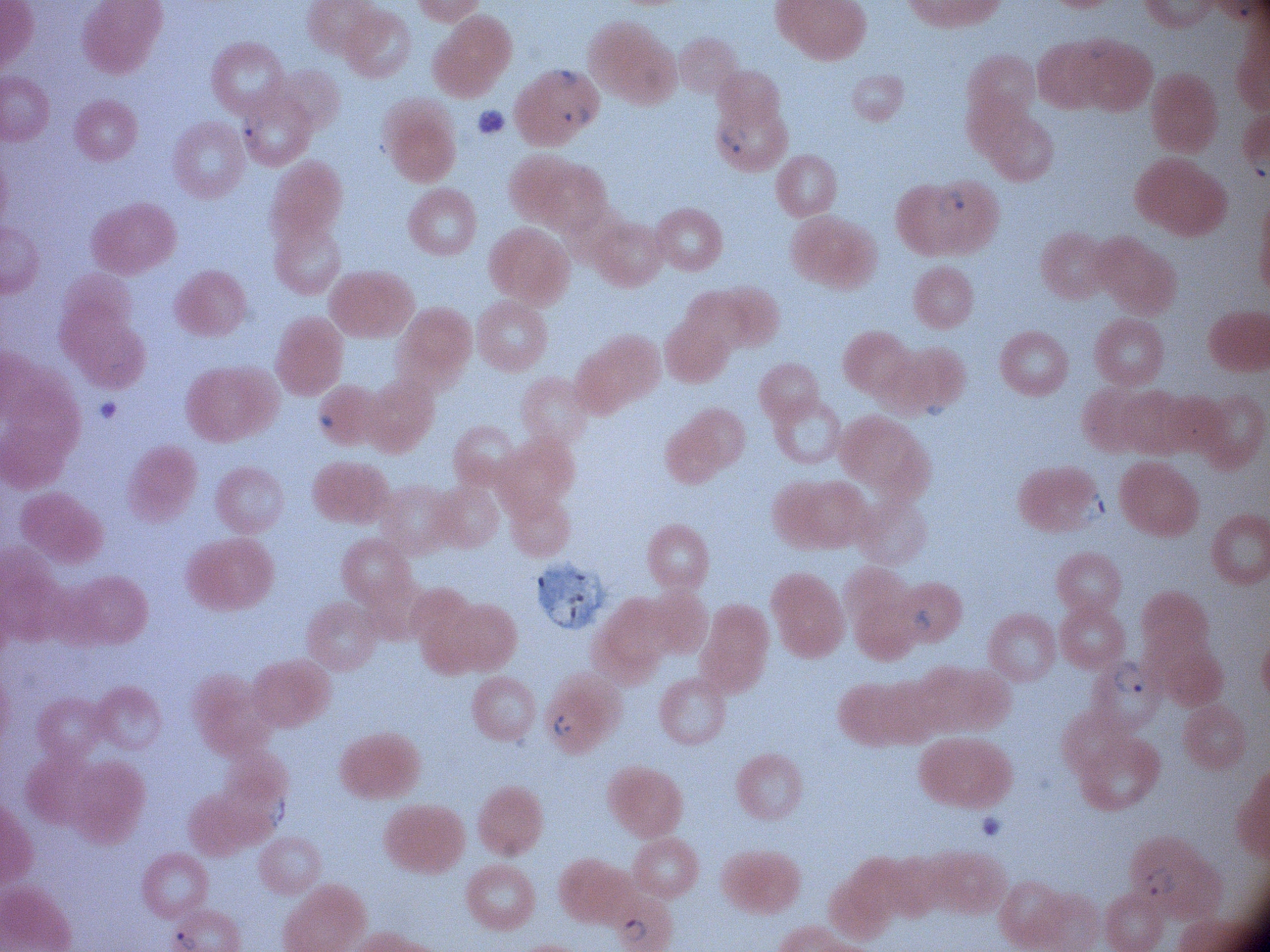

field of view = one from this slide
preparation = thin blood film
ring form locations = approximate bounding boxes as named x1/y1/x2/y2 corners in pixels, from the source annotation, which is not necessarily exhaustive: (x1=548, y1=63, x2=580, y2=91), (x1=562, y1=103, x2=590, y2=129), (x1=237, y1=112, x2=265, y2=150), (x1=715, y1=122, x2=748, y2=155), (x1=933, y1=186, x2=967, y2=220), (x1=1081, y1=490, x2=1109, y2=523), (x1=1111, y1=658, x2=1147, y2=697), (x1=549, y1=709, x2=575, y2=741), (x1=262, y1=794, x2=293, y2=831), (x1=1140, y1=865, x2=1178, y2=901), (x1=620, y1=913, x2=649, y2=942)
magnification = 100x
microscope = Leica DM2000 with built-in camera
species = Plasmodium falciparum
stain = Giemsa
image size = 1270×952 pixels